Name the parasite shown.
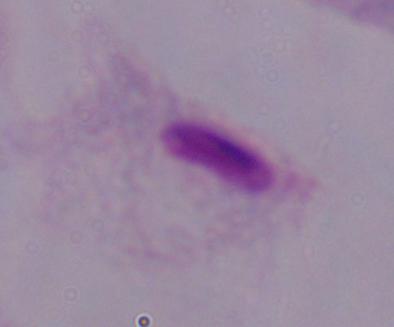

This is a trichomonad.

modality = micrograph
magnification = 1000x